Assess the morphology of the red blood cells.
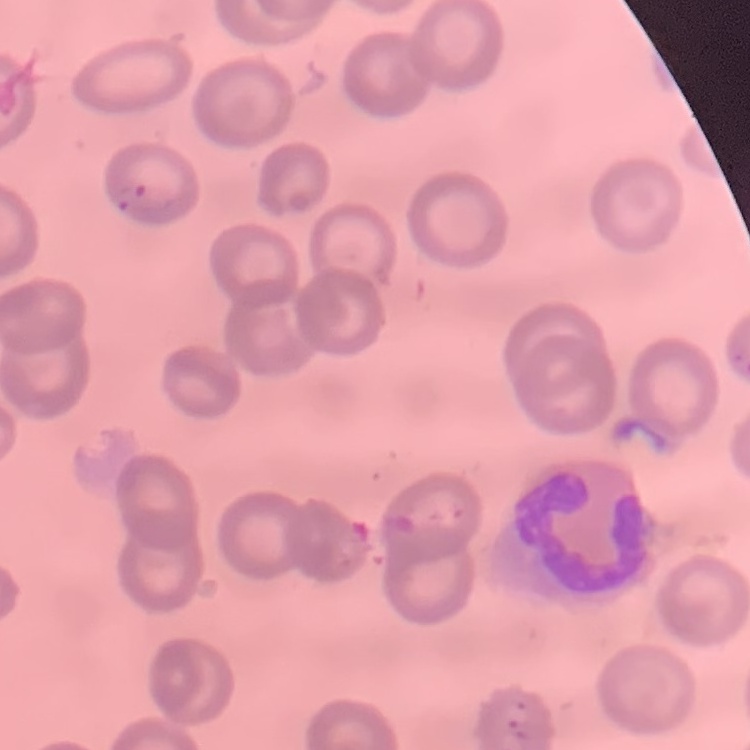
They show no rouleaux formation.

Summary:
  - Image type: square crop of a larger photomicrograph
  - Preparation: thin blood film
  - Stain: Field's or Giemsa